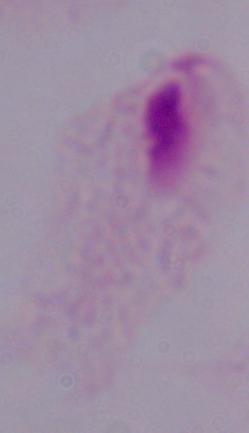

Summary:
  - Identification: trichomonad
  - Magnification: 1000x
  - Modality: micrograph